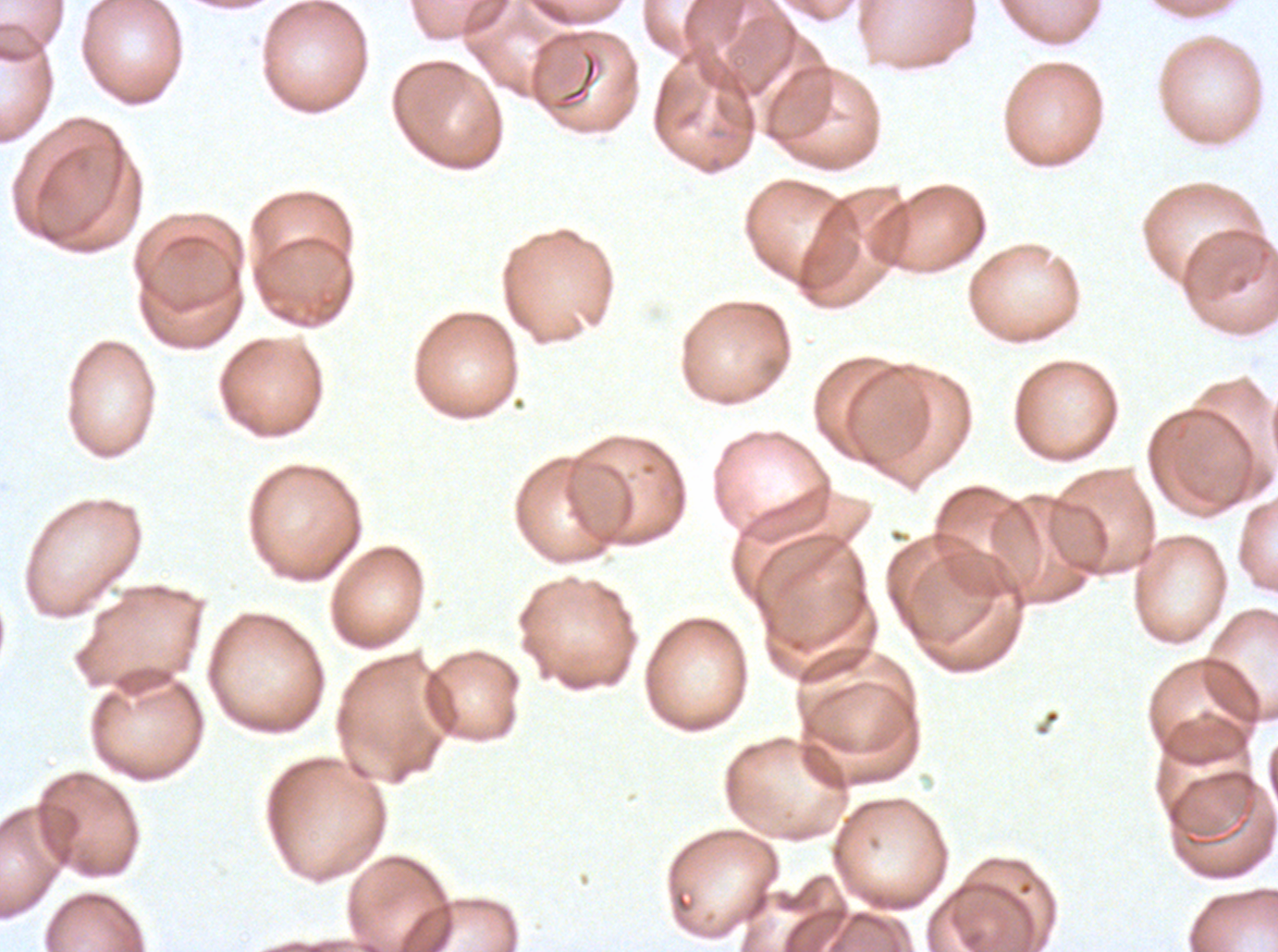
preparation: thin blood smear
specimen: P. falciparum cultured ex vivo for 24 to 48 hours, from a patient in The Gambia
debris_locations: 'approximate bounding boxes as (x1, y1, x2, y2) in pixels: (552, 47, 602, 111)'
stain: Giemsa
field_of_view: one sub-image of a larger composite
image_size: 1278×952 pixels